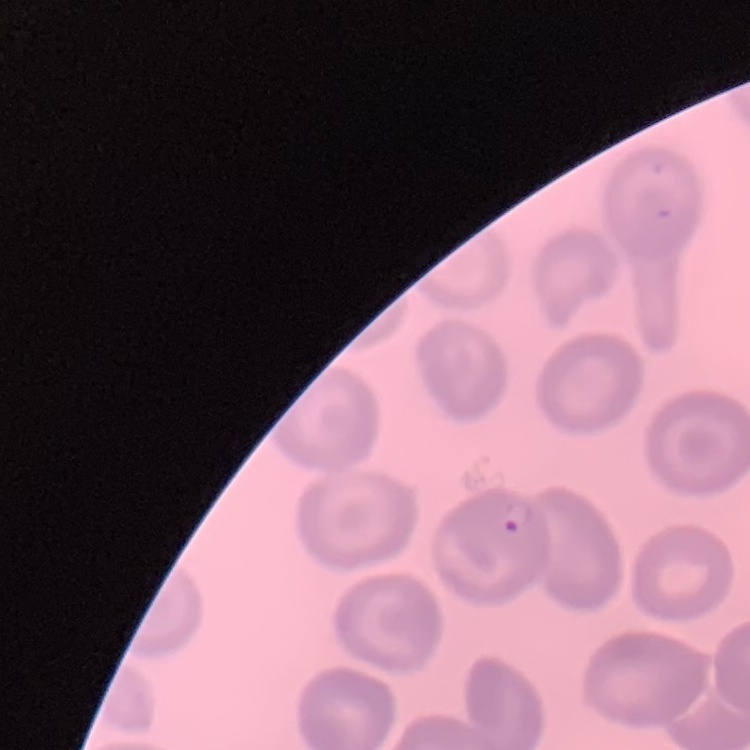 The red blood cells show no rouleaux formation. Field's or Giemsa stain. Thin peripheral smear. Square crop of a larger photomicrograph.